Classify this cell by malaria status.
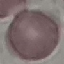

It is uninfected.

Summary:
  - Image type: cell patch, automatically extracted from a larger field of view and resized to 64 × 64 pixels
  - Preparation: thin blood smear
  - Capture: smartphone through the microscope eyepiece
  - Stain: Giemsa